Name the cell type shown.
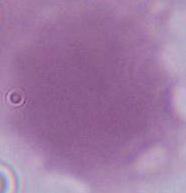

This is an erythrocyte.

Photomicrograph. Captured at 1000x magnification.